Give the extent of all Plasmodium falciparum-infected red blood cells.
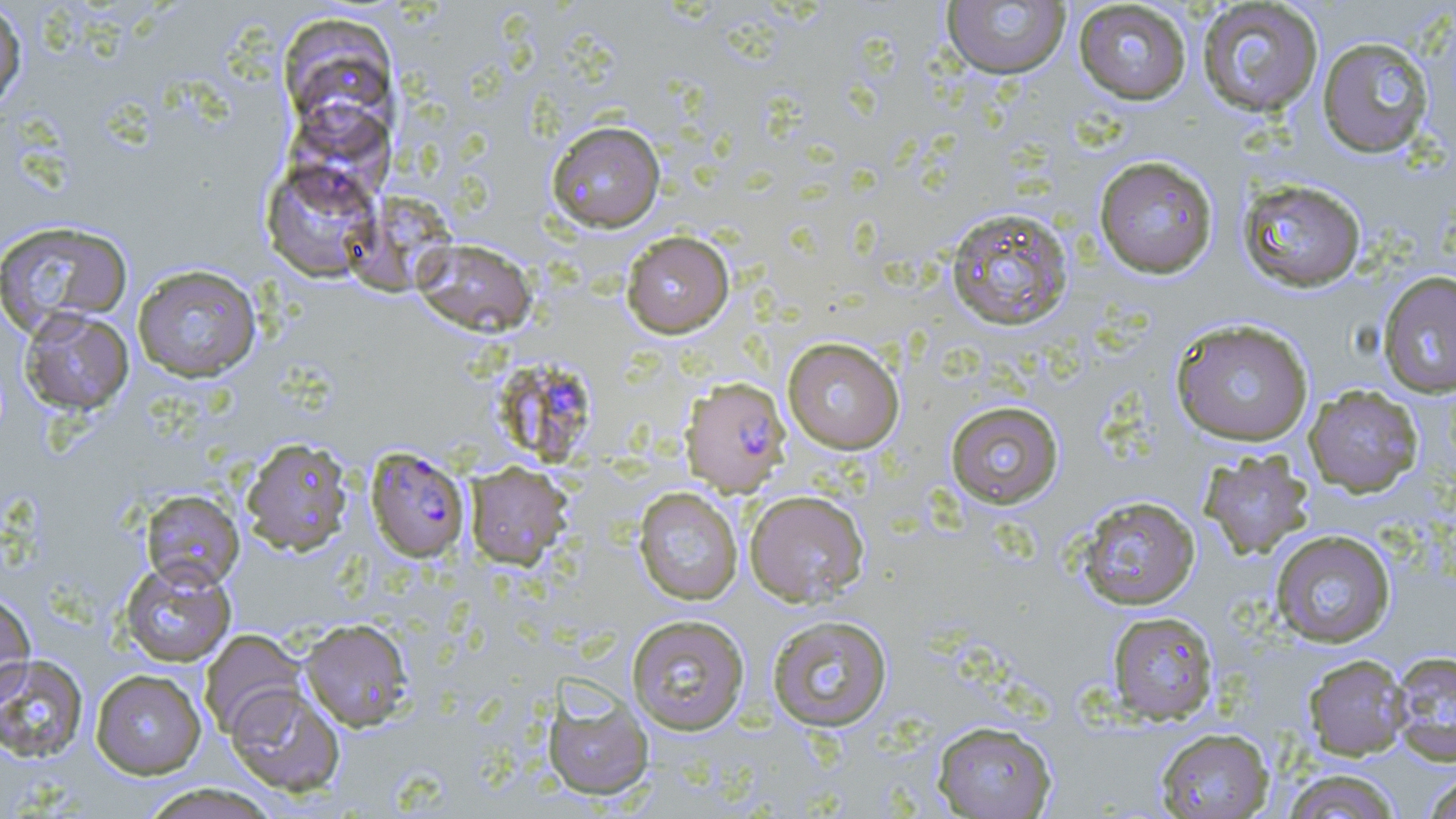

Approximate bounding boxes as [x1, y1, x2, y2] in pixels.
Plasmodium falciparum-infected red blood cells: [491, 363, 599, 468], [681, 376, 791, 496], [366, 447, 471, 562].

Summary:
  - Uninfected red blood cell locations: [1073, 1, 1192, 104], [1196, 1, 1324, 117], [0, 2, 27, 114], [940, 2, 1071, 79], [278, 14, 398, 129], [1317, 36, 1435, 158], [546, 120, 666, 233], [1093, 155, 1219, 279], [261, 159, 381, 282], [1237, 178, 1367, 293], [944, 205, 1074, 332], [0, 220, 133, 336], [621, 230, 734, 338], [413, 238, 537, 337], [132, 264, 262, 382], [1377, 271, 1456, 399], [19, 308, 134, 415], [1170, 318, 1315, 447], [782, 337, 904, 454], [1304, 384, 1423, 497], [945, 400, 1064, 508], [240, 436, 354, 557], [1199, 450, 1314, 559], [465, 462, 571, 569], [633, 487, 743, 605], [140, 489, 244, 591], [744, 489, 870, 607], [1074, 495, 1201, 610], [1270, 529, 1396, 648], [118, 560, 236, 667], [0, 591, 36, 706], [1107, 611, 1219, 724], [626, 613, 751, 735], [766, 614, 893, 732], [299, 618, 414, 731], [198, 629, 306, 738], [1389, 650, 1456, 765], [0, 654, 89, 763], [1303, 654, 1410, 760], [90, 669, 207, 779], [541, 681, 655, 801], [226, 684, 346, 797], [932, 720, 1057, 818], [1155, 727, 1274, 818], [1280, 768, 1404, 819], [1422, 771, 1456, 819], [138, 783, 280, 819]
  - Slide-level diagnosis: Plasmodium falciparum
  - Preparation: thin blood film
  - Field of view: one of a larger specimen
  - Stain: May-Grünwald-Giemsa
  - Image size: 1456×819 pixels
  - Modality: light microscopy
  - Magnification: 1000x